Identify the blood parasite species.
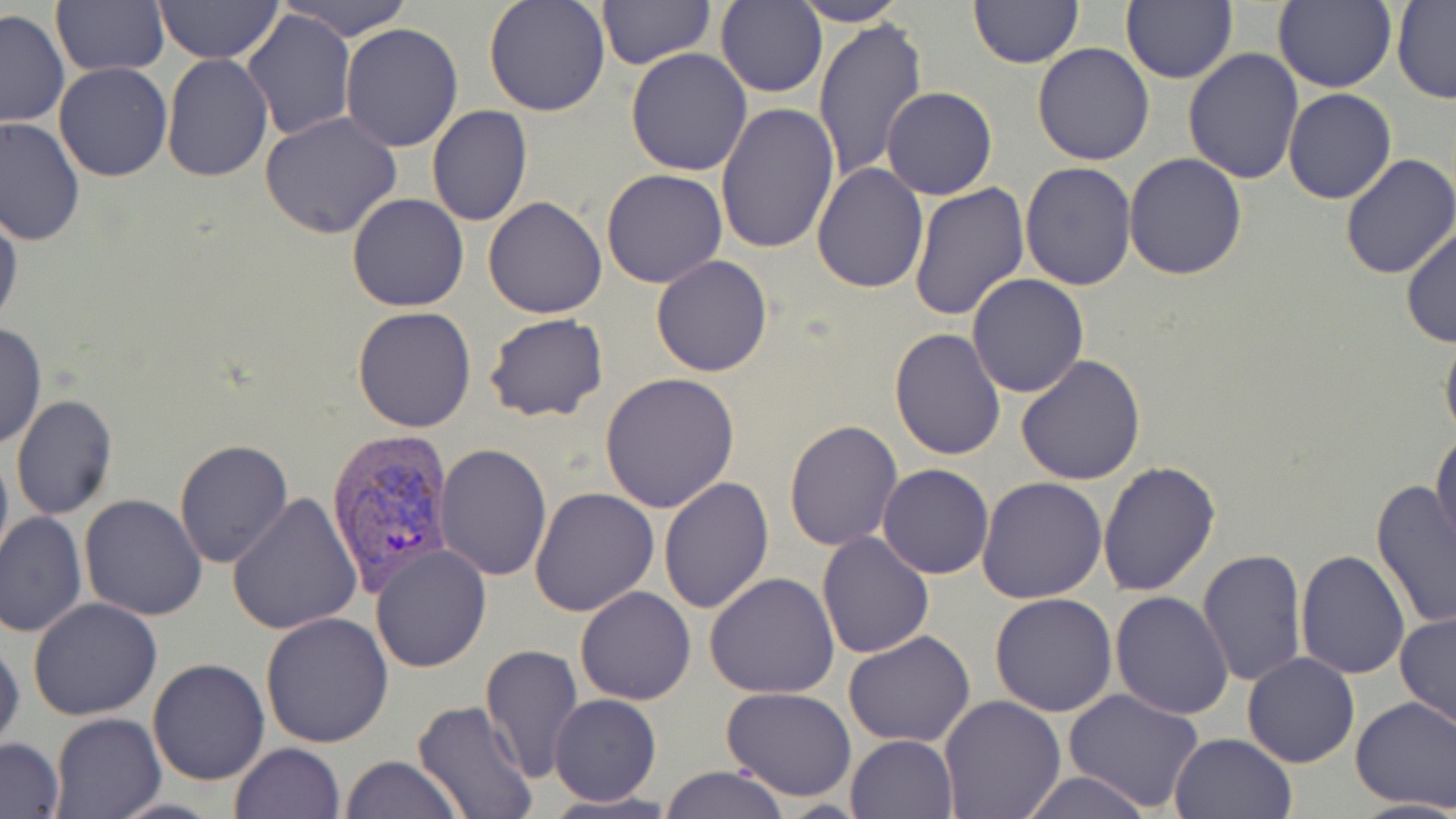
Plasmodium vivax.

Approximate bounding boxes as named x1/y1/x2/y2 corners in pixels. Uninfected red blood cell locations: (x1=153, y1=0, x2=283, y2=63), (x1=280, y1=0, x2=417, y2=42), (x1=483, y1=0, x2=611, y2=117), (x1=596, y1=0, x2=714, y2=69), (x1=1120, y1=0, x2=1236, y2=86), (x1=1392, y1=0, x2=1456, y2=104), (x1=50, y1=1, x2=169, y2=77), (x1=968, y1=1, x2=1084, y2=68), (x1=1273, y1=1, x2=1397, y2=93), (x1=716, y1=2, x2=828, y2=98), (x1=790, y1=2, x2=908, y2=26), (x1=0, y1=10, x2=69, y2=126), (x1=242, y1=10, x2=356, y2=142), (x1=813, y1=16, x2=928, y2=184), (x1=339, y1=22, x2=464, y2=151), (x1=1032, y1=42, x2=1156, y2=165), (x1=1184, y1=47, x2=1306, y2=184), (x1=624, y1=48, x2=752, y2=176), (x1=162, y1=53, x2=273, y2=183), (x1=55, y1=62, x2=174, y2=182), (x1=883, y1=86, x2=998, y2=199), (x1=1282, y1=89, x2=1396, y2=204), (x1=714, y1=103, x2=838, y2=256), (x1=427, y1=105, x2=531, y2=225), (x1=260, y1=110, x2=402, y2=239), (x1=0, y1=118, x2=84, y2=247), (x1=1124, y1=152, x2=1249, y2=281), (x1=1338, y1=154, x2=1456, y2=280), (x1=811, y1=162, x2=929, y2=293), (x1=1020, y1=162, x2=1136, y2=291), (x1=602, y1=169, x2=727, y2=288), (x1=909, y1=184, x2=1031, y2=321), (x1=347, y1=194, x2=468, y2=312), (x1=482, y1=196, x2=608, y2=319), (x1=0, y1=200, x2=23, y2=334), (x1=1402, y1=224, x2=1456, y2=349), (x1=651, y1=254, x2=773, y2=377), (x1=967, y1=273, x2=1090, y2=397), (x1=351, y1=306, x2=477, y2=431), (x1=484, y1=314, x2=607, y2=424), (x1=0, y1=321, x2=46, y2=452), (x1=1440, y1=327, x2=1456, y2=449), (x1=889, y1=328, x2=1006, y2=460), (x1=1015, y1=355, x2=1148, y2=485), (x1=600, y1=372, x2=739, y2=511), (x1=11, y1=396, x2=118, y2=520), (x1=785, y1=420, x2=903, y2=552), (x1=1431, y1=427, x2=1456, y2=556), (x1=0, y1=437, x2=13, y2=571), (x1=173, y1=440, x2=294, y2=570), (x1=436, y1=443, x2=553, y2=581), (x1=1096, y1=460, x2=1222, y2=598), (x1=878, y1=464, x2=993, y2=580), (x1=659, y1=477, x2=773, y2=615), (x1=976, y1=478, x2=1107, y2=604), (x1=1371, y1=480, x2=1455, y2=630), (x1=529, y1=485, x2=659, y2=616), (x1=228, y1=492, x2=362, y2=635), (x1=79, y1=494, x2=207, y2=622), (x1=1, y1=512, x2=86, y2=639), (x1=816, y1=530, x2=935, y2=659), (x1=370, y1=544, x2=492, y2=671), (x1=1197, y1=548, x2=1306, y2=688), (x1=1295, y1=551, x2=1410, y2=680), (x1=704, y1=572, x2=841, y2=699), (x1=576, y1=585, x2=696, y2=706), (x1=1110, y1=592, x2=1234, y2=719), (x1=988, y1=593, x2=1118, y2=717), (x1=28, y1=597, x2=163, y2=720), (x1=1396, y1=611, x2=1456, y2=734), (x1=260, y1=612, x2=393, y2=748), (x1=843, y1=630, x2=976, y2=747), (x1=0, y1=636, x2=24, y2=760), (x1=480, y1=644, x2=583, y2=780), (x1=1242, y1=653, x2=1361, y2=768), (x1=148, y1=658, x2=270, y2=785), (x1=720, y1=686, x2=858, y2=800), (x1=1064, y1=689, x2=1205, y2=814), (x1=549, y1=694, x2=661, y2=807), (x1=938, y1=694, x2=1067, y2=819), (x1=1350, y1=696, x2=1456, y2=814), (x1=412, y1=701, x2=538, y2=819), (x1=50, y1=714, x2=164, y2=819), (x1=1168, y1=733, x2=1296, y2=819), (x1=845, y1=734, x2=959, y2=819), (x1=0, y1=737, x2=65, y2=817), (x1=230, y1=743, x2=345, y2=819), (x1=341, y1=755, x2=462, y2=819), (x1=657, y1=765, x2=788, y2=819), (x1=1015, y1=771, x2=1153, y2=819), (x1=537, y1=790, x2=682, y2=819). Plasmodium vivax-infected red blood cell locations: (x1=324, y1=428, x2=454, y2=597). Single field of view. Light microscopy. Captured at 1000x magnification. Thin blood film. Image is 1456×819 pixels. May-Grünwald-Giemsa-stained preparation.